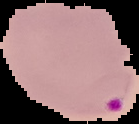

preparation = thin blood film
malaria status = parasitized
image type = segmented cell region on a black background
image size = 139×124 pixels